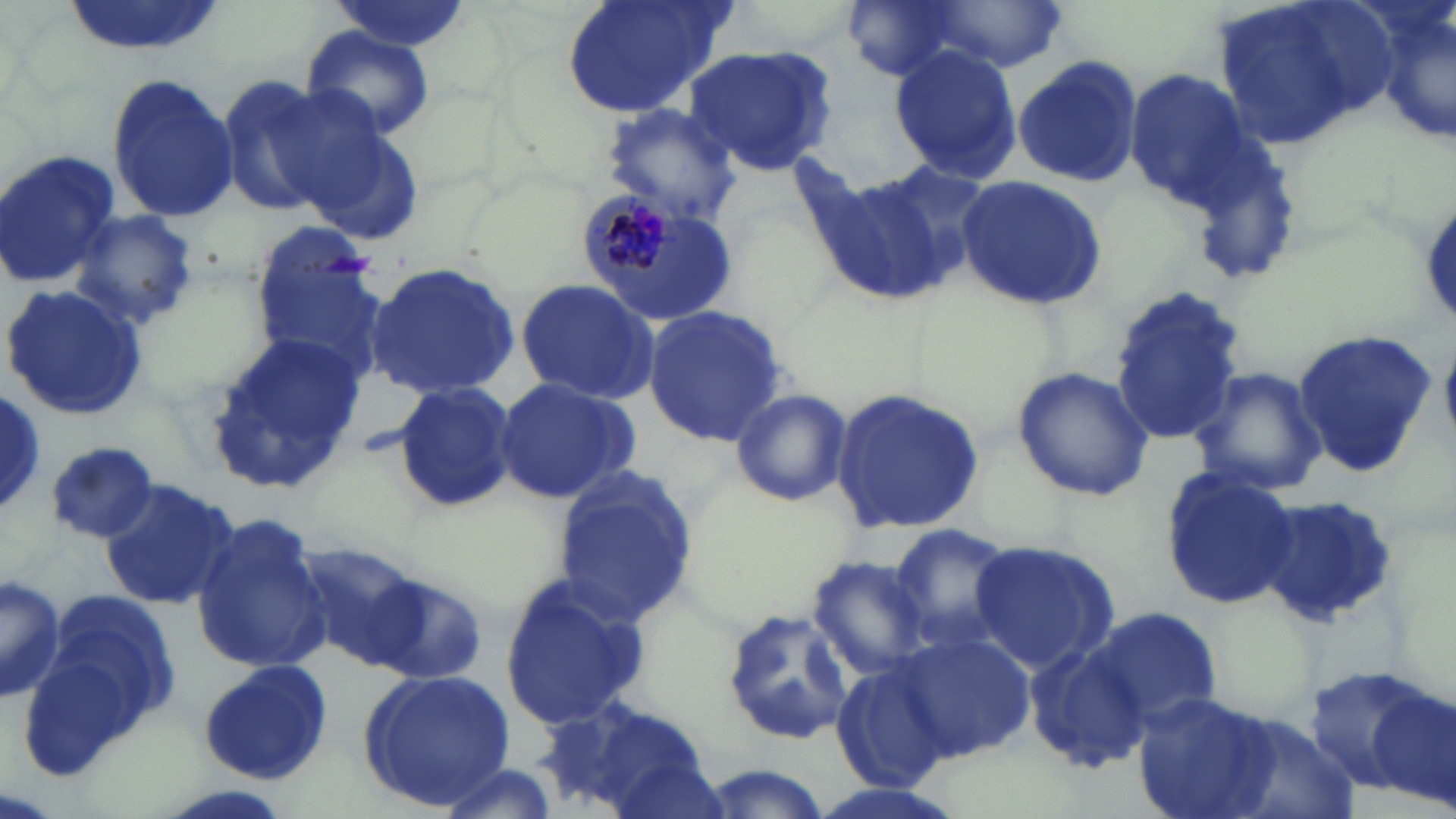
slide_level_diagnosis: Plasmodium malariae
modality: optical microscopy
preparation: thin blood film
magnification: 1000x
stain: May-Grünwald-Giemsa
image_size: 1456×819 pixels
field_of_view: single
plasmodium_malariae_infected_red_blood_cell_locations: 'approximate bounding boxes as named x1/y1/x2/y2 corners in pixels: (x1=579, y1=183, x2=691, y2=299)'
uninfected_red_blood_cell_locations: 'approximate bounding boxes as named x1/y1/x2/y2 corners in pixels: (x1=59, y1=0, x2=230, y2=59), (x1=560, y1=0, x2=735, y2=122), (x1=839, y1=0, x2=978, y2=84), (x1=1207, y1=0, x2=1395, y2=151), (x1=1368, y1=0, x2=1455, y2=142), (x1=326, y1=1, x2=475, y2=55), (x1=918, y1=3, x2=1068, y2=72), (x1=298, y1=27, x2=437, y2=142), (x1=680, y1=46, x2=837, y2=176), (x1=887, y1=46, x2=1023, y2=181), (x1=1013, y1=56, x2=1143, y2=186), (x1=1122, y1=67, x2=1264, y2=213), (x1=107, y1=71, x2=237, y2=223), (x1=217, y1=76, x2=338, y2=216), (x1=600, y1=103, x2=742, y2=224), (x1=301, y1=126, x2=426, y2=247), (x1=0, y1=147, x2=119, y2=287), (x1=863, y1=159, x2=996, y2=290), (x1=811, y1=172, x2=951, y2=303), (x1=955, y1=174, x2=1106, y2=311), (x1=71, y1=211, x2=199, y2=330), (x1=251, y1=230, x2=388, y2=377), (x1=364, y1=263, x2=523, y2=398), (x1=514, y1=277, x2=662, y2=405), (x1=4, y1=284, x2=150, y2=420), (x1=1109, y1=284, x2=1246, y2=445), (x1=642, y1=303, x2=789, y2=449), (x1=1291, y1=327, x2=1434, y2=475), (x1=206, y1=337, x2=367, y2=489), (x1=1012, y1=366, x2=1155, y2=504), (x1=1190, y1=366, x2=1328, y2=497), (x1=493, y1=376, x2=638, y2=504), (x1=392, y1=380, x2=517, y2=512), (x1=830, y1=386, x2=985, y2=536), (x1=728, y1=387, x2=852, y2=508), (x1=0, y1=394, x2=47, y2=514), (x1=46, y1=430, x2=160, y2=544), (x1=550, y1=463, x2=701, y2=627), (x1=1159, y1=468, x2=1297, y2=611), (x1=100, y1=480, x2=240, y2=610), (x1=1256, y1=499, x2=1399, y2=626), (x1=189, y1=511, x2=334, y2=675), (x1=887, y1=522, x2=1016, y2=651), (x1=289, y1=537, x2=428, y2=667), (x1=969, y1=538, x2=1120, y2=675), (x1=806, y1=553, x2=934, y2=679), (x1=499, y1=572, x2=655, y2=732), (x1=0, y1=573, x2=63, y2=704), (x1=368, y1=575, x2=486, y2=684), (x1=23, y1=594, x2=185, y2=772), (x1=721, y1=606, x2=856, y2=744), (x1=1086, y1=607, x2=1222, y2=727), (x1=893, y1=631, x2=1036, y2=760), (x1=1020, y1=642, x2=1147, y2=773), (x1=196, y1=658, x2=333, y2=786), (x1=831, y1=660, x2=959, y2=793), (x1=1305, y1=663, x2=1444, y2=797), (x1=357, y1=667, x2=515, y2=809), (x1=1367, y1=686, x2=1456, y2=807), (x1=1131, y1=692, x2=1279, y2=819), (x1=538, y1=696, x2=712, y2=819), (x1=1220, y1=707, x2=1364, y2=818), (x1=430, y1=760, x2=563, y2=819), (x1=694, y1=765, x2=834, y2=818)'